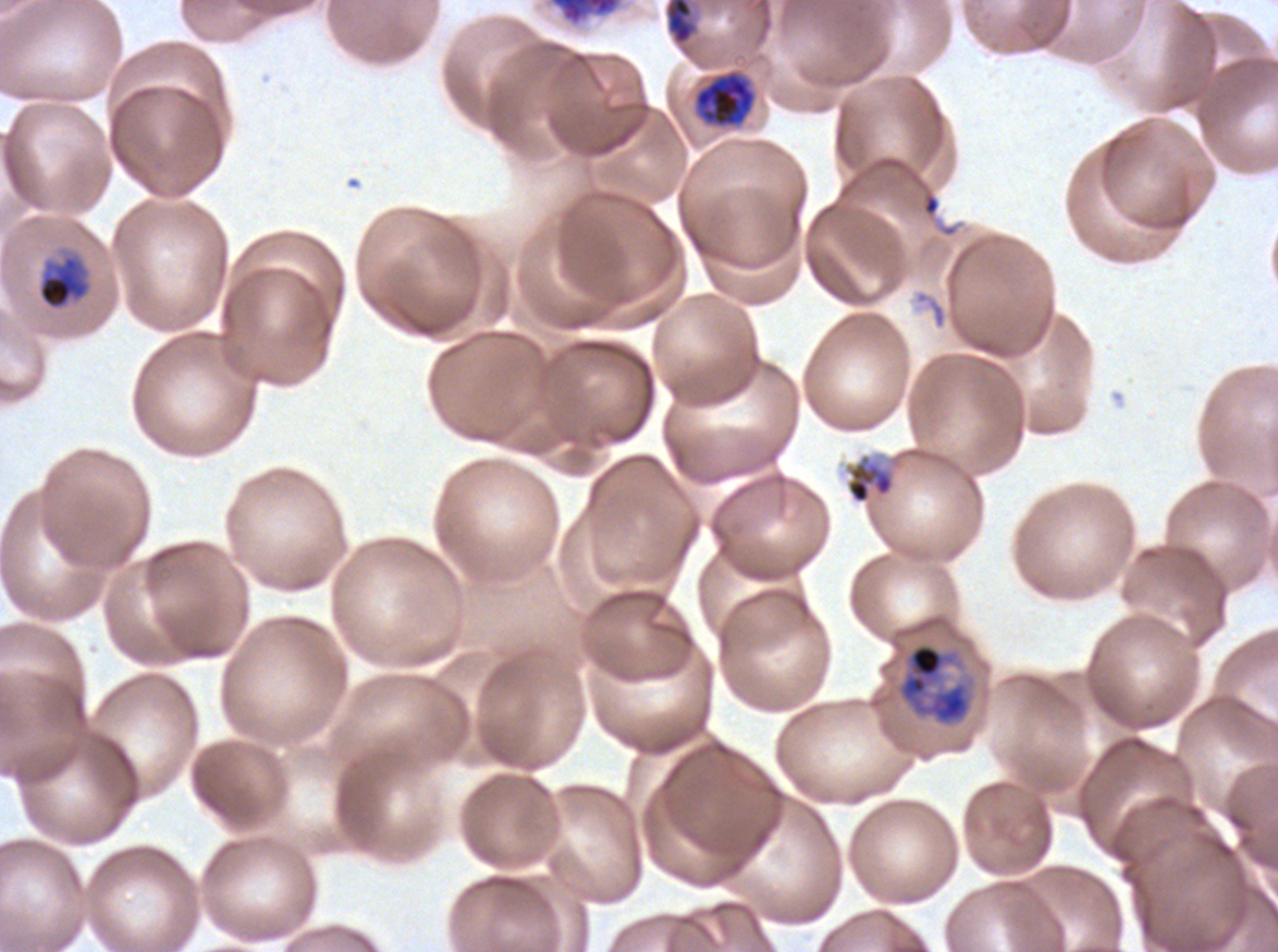
Approximate bounding boxes as {x1, y1, x2, y2} in pixels.
Summary:
  - Debris locations: {923, 195, 940, 215}
  - Late trophozoite locations: {663, 0, 701, 55}, {694, 71, 756, 127}
  - Early schizont locations: {548, 0, 622, 27}, {894, 641, 976, 728}
  - Mid trophozoite locations: {37, 253, 92, 311}, {844, 452, 896, 505}
  - Life-cycle stages observed: mid trophozoite, late trophozoite, early schizont
  - Field of view: sub-image separated from a larger composite
  - Preparation: thin blood film
  - Image size: 1278×952 pixels
  - Stain: Giemsa
  - Specimen: P. falciparum cultured ex vivo for 24 to 48 hours, from a patient in The Gambia